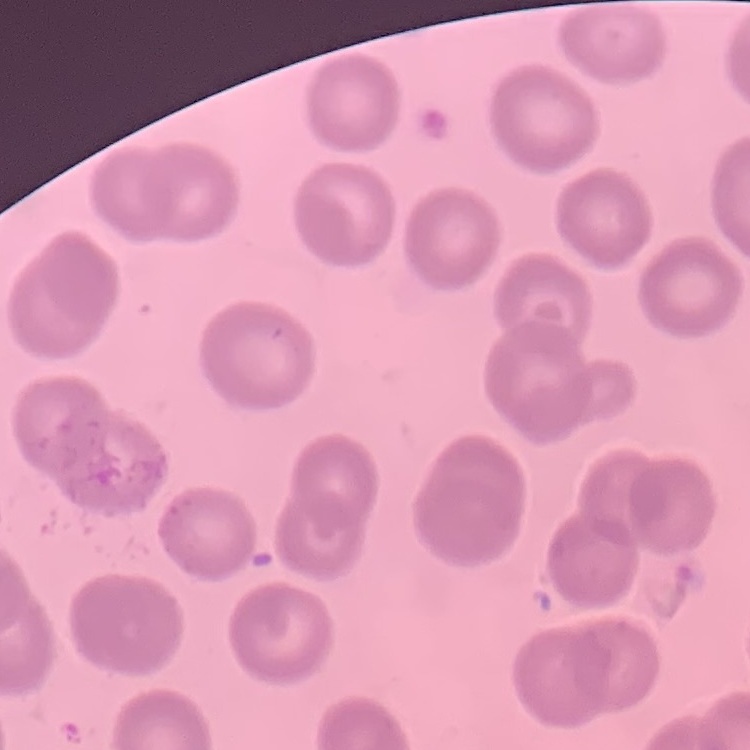

erythrocyte morphology = no rouleaux formation
image type = square crop of a larger photomicrograph
preparation = thin blood smear
stain = Field's or Giemsa